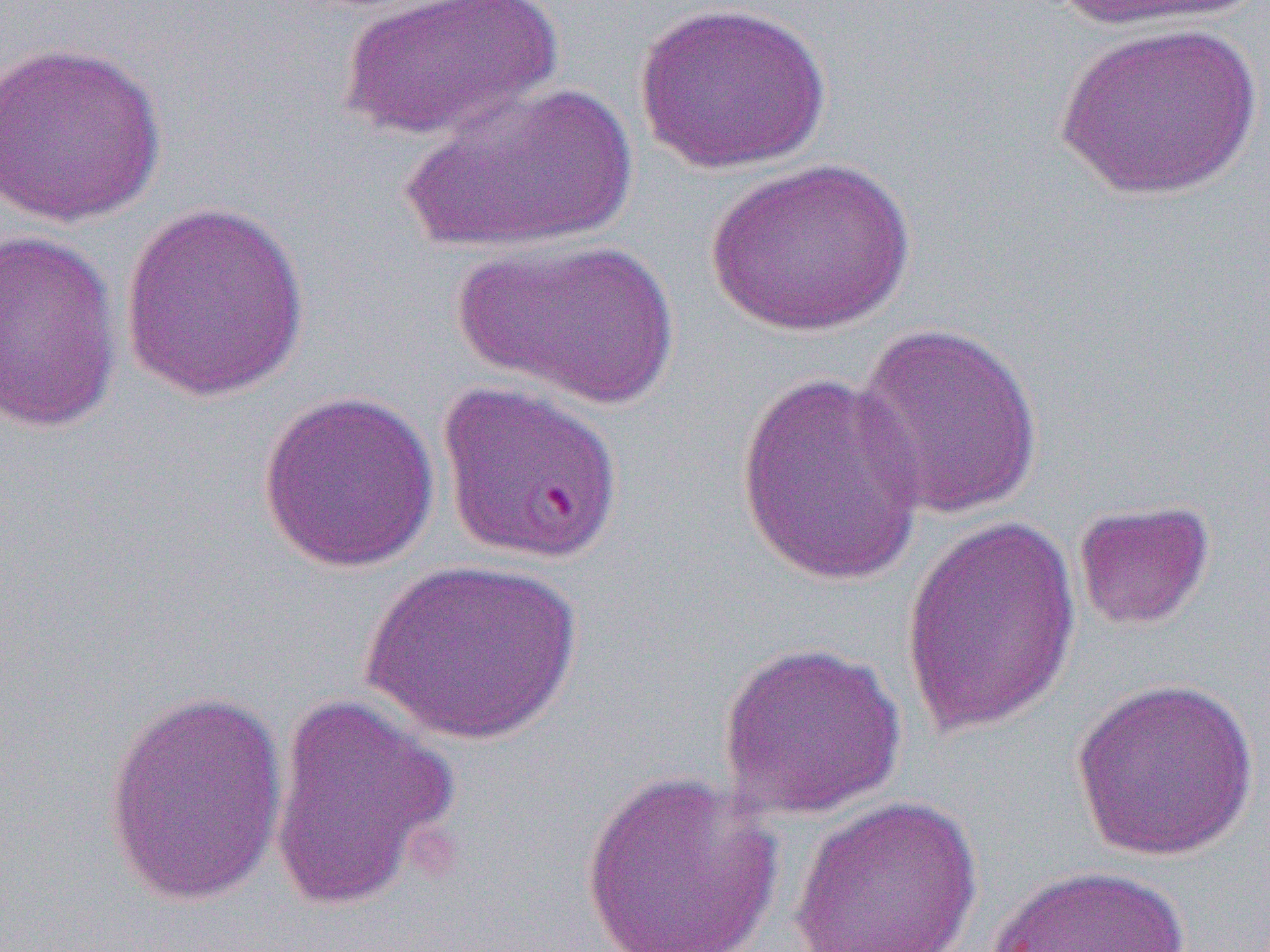

slide-level diagnosis = Plasmodium falciparum
modality = light microscopy
magnification = 1000x
field of view = single
image size = 1270×952 pixels
uninfected red blood cell locations = approximate bounding boxes as (x1, y1, x2, y2) in pixels: (342, 0, 561, 142), (1047, 0, 1257, 33), (634, 1, 833, 175), (1054, 20, 1264, 202), (0, 40, 168, 227), (398, 80, 638, 256), (706, 158, 915, 336), (118, 201, 311, 401), (0, 228, 125, 436), (452, 236, 679, 411), (852, 322, 1045, 522), (735, 371, 929, 588), (436, 381, 623, 566), (257, 389, 441, 574), (1073, 498, 1215, 632), (899, 512, 1083, 737), (361, 559, 583, 746), (717, 639, 909, 820), (1070, 677, 1260, 862), (103, 688, 289, 907), (266, 691, 463, 915), (580, 769, 783, 951), (787, 795, 984, 952), (986, 864, 1193, 952)
preparation = thin blood smear